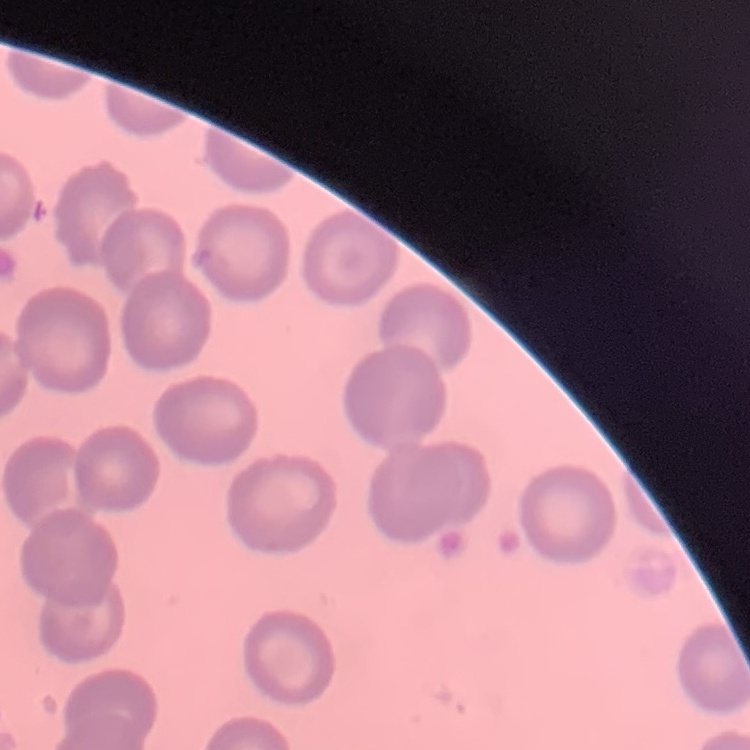

Summary:
  - Red blood cell morphology: no rouleaux formation
  - Image type: square crop of a larger photomicrograph
  - Preparation: thin peripheral smear
  - Stain: Field's or Giemsa